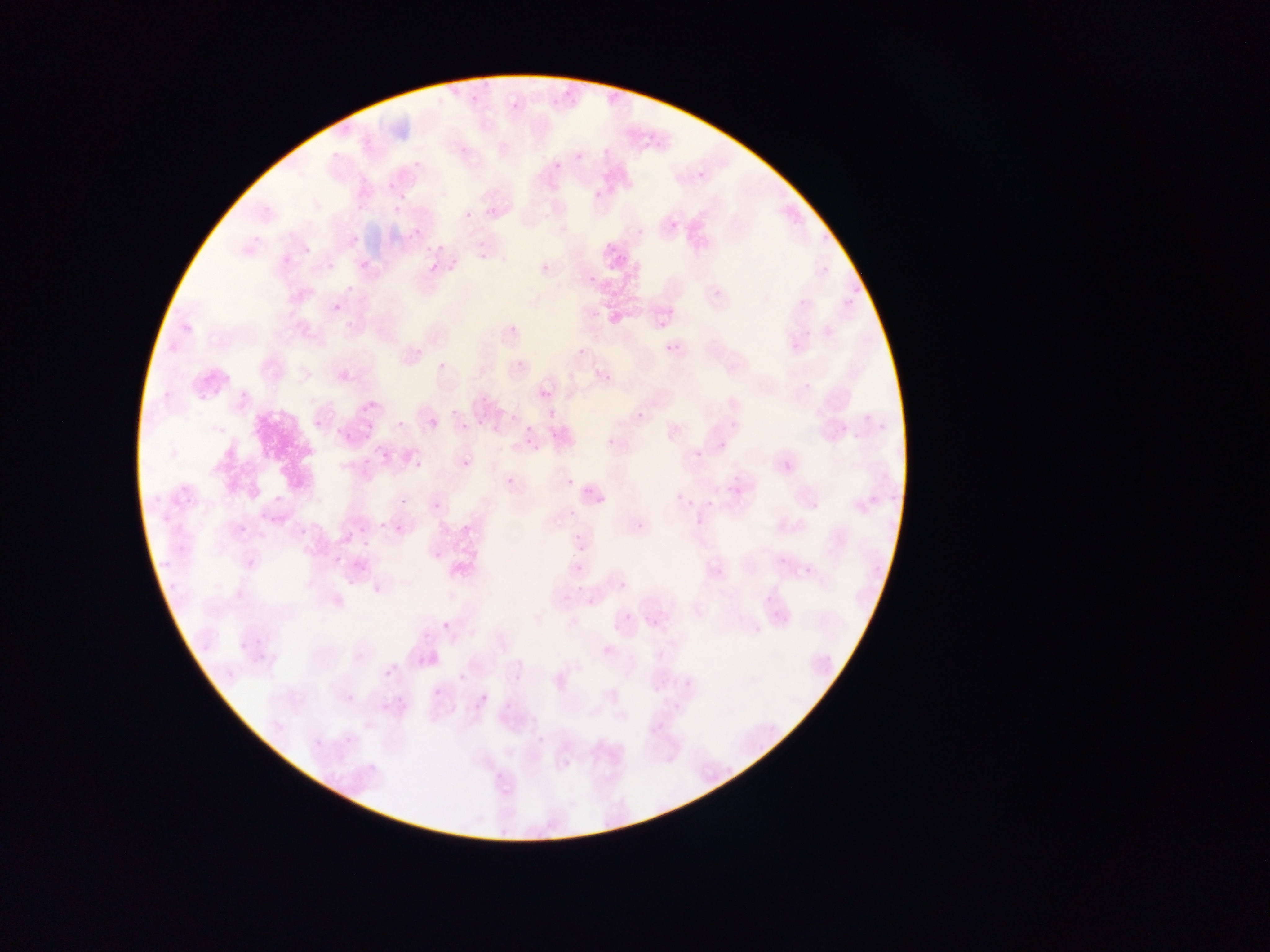

Approximate bounding boxes as left top right bottom in pixels. Plasmodium parasite locations: 469 88 479 102; 562 88 574 97; 511 97 521 109; 549 97 559 105; 640 121 656 146; 602 140 618 157; 575 144 587 162; 551 152 564 171; 693 168 704 180; 387 182 395 190; 592 183 605 197; 392 206 402 215; 463 207 476 219; 670 220 679 229; 411 228 422 238; 636 228 644 236; 349 236 359 245; 431 242 445 249; 478 242 498 271; 604 245 613 254; 301 246 311 256; 446 250 462 269; 360 259 372 270; 539 260 547 270; 326 261 334 272; 429 263 439 273; 587 276 595 285; 848 280 864 303; 330 301 342 314; 504 318 522 332; 659 320 667 328; 414 339 427 362; 574 343 587 358; 665 344 675 352; 510 355 521 367; 436 361 447 371; 600 364 614 386; 800 372 817 394; 540 389 552 401; 360 393 380 414; 632 406 642 417; 450 407 456 415; 859 412 873 424; 310 413 319 427; 508 413 517 421; 475 414 484 426; 876 416 887 430; 398 418 408 428; 429 419 438 429; 363 421 376 443; 461 422 470 430; 525 425 534 433; 851 427 864 439; 605 428 616 449; 339 429 351 440; 546 430 556 439; 524 437 535 447; 694 450 703 458; 379 451 389 461; 780 452 792 472; 461 457 472 469; 361 458 372 468; 413 460 423 469; 730 475 742 492; 502 478 517 482; 566 478 575 487; 582 486 591 494; 401 491 410 504; 272 493 284 505; 676 493 683 501; 593 495 606 503; 431 497 439 511; 688 498 696 506; 706 499 715 511; 381 509 392 530; 567 511 577 520; 631 518 649 535; 238 523 248 534; 395 523 406 534; 356 524 370 535; 297 526 308 538; 573 532 581 541; 361 539 371 548; 431 547 443 560; 333 555 343 565; 777 556 782 564; 572 562 581 573; 799 567 809 575; 342 569 360 592; 617 576 631 590; 574 583 581 595; 372 584 383 595; 764 588 776 604; 583 596 598 609; 771 607 785 616; 646 610 657 628; 619 612 632 620; 443 619 449 631; 611 622 618 634; 752 622 763 635; 256 626 268 645; 236 642 245 651; 384 666 395 677; 458 673 468 683; 513 673 522 683; 433 687 442 697; 347 689 357 704; 478 693 489 705; 504 702 514 712; 377 703 387 709; 648 709 672 736; 312 732 324 748; 345 732 356 748; 562 758 571 769. Collected in Ghana. Image is 1270×952 pixels. Thin blood smear. Single field of view. Photographed through a microscope with a mobile-phone camera.